Give the position of every malaria parasite.
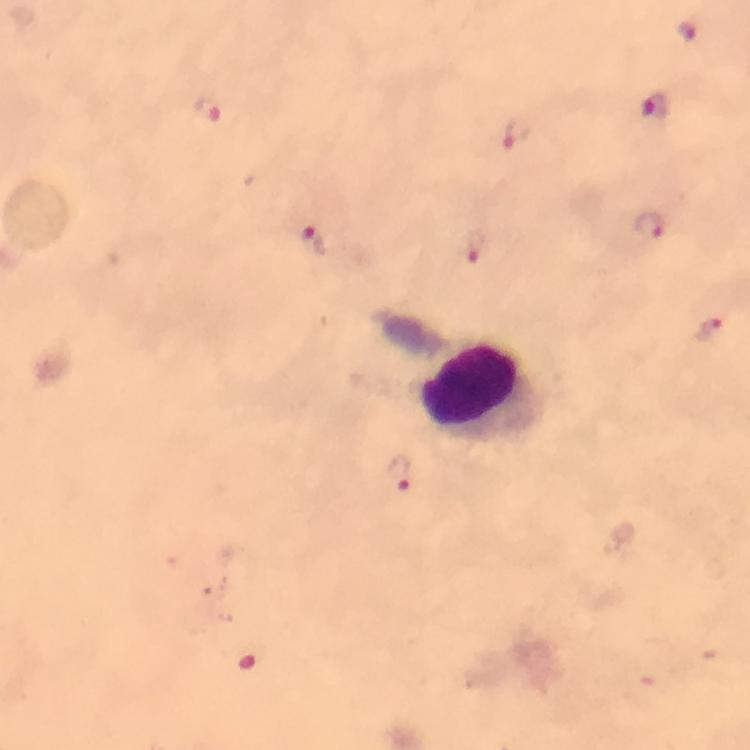

Approximate centers as {x, y} in pixels.
Malaria parasites: {685, 31}, {655, 106}, {203, 107}, {515, 132}, {648, 226}, {313, 243}, {475, 243}, {708, 331}, {401, 473}.

{
  "image_size": "750×750 pixels",
  "cropped_from": "one field of view",
  "stain": "Giemsa",
  "context": "from a malaria diagnostic workup",
  "leukocyte_locations": "approximate centers as {x, y} in pixels: {479, 391}",
  "capture": "smartphone camera through the microscope",
  "preparation": "thick blood smear",
  "immersion_oil": "used",
  "magnification": "100x"
}